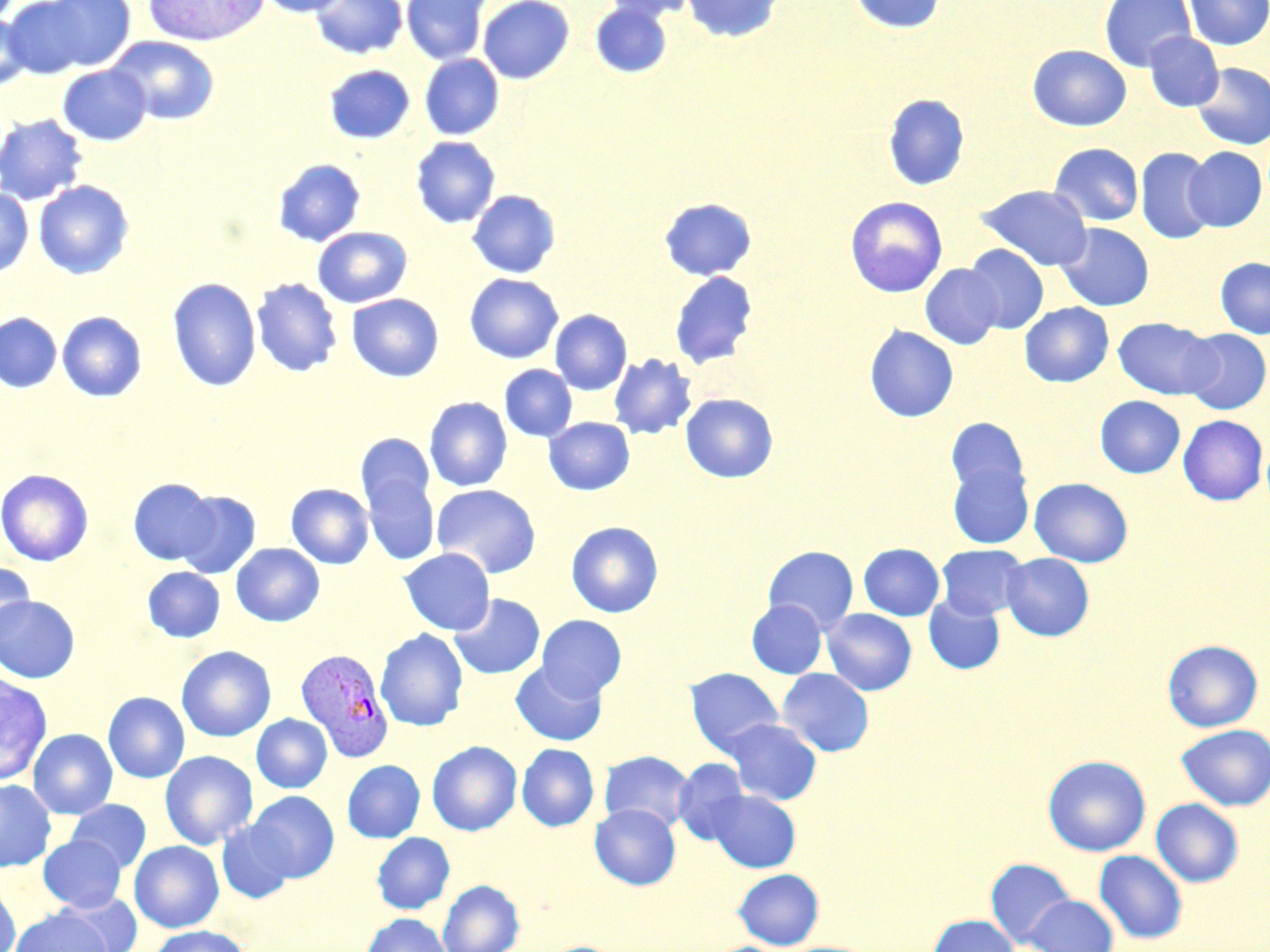

slide-level diagnosis = Plasmodium vivax
uninfected red blood cell locations = approximate bounding boxes as named x1/y1/x2/y2 corners in pixels: (x1=10, y1=0, x2=137, y2=75), (x1=143, y1=0, x2=268, y2=47), (x1=257, y1=0, x2=351, y2=17), (x1=310, y1=0, x2=407, y2=59), (x1=402, y1=0, x2=490, y2=65), (x1=478, y1=0, x2=574, y2=84), (x1=601, y1=0, x2=699, y2=22), (x1=681, y1=0, x2=785, y2=43), (x1=847, y1=0, x2=947, y2=35), (x1=1099, y1=0, x2=1195, y2=71), (x1=1183, y1=0, x2=1269, y2=51), (x1=589, y1=3, x2=672, y2=79), (x1=0, y1=12, x2=33, y2=89), (x1=1145, y1=32, x2=1224, y2=112), (x1=107, y1=36, x2=220, y2=125), (x1=1027, y1=44, x2=1131, y2=131), (x1=420, y1=54, x2=504, y2=140), (x1=1192, y1=62, x2=1270, y2=150), (x1=324, y1=64, x2=415, y2=144), (x1=58, y1=65, x2=152, y2=145), (x1=882, y1=93, x2=970, y2=191), (x1=0, y1=113, x2=89, y2=206), (x1=410, y1=136, x2=500, y2=228), (x1=1049, y1=143, x2=1144, y2=226), (x1=1183, y1=146, x2=1267, y2=231), (x1=1135, y1=147, x2=1217, y2=244), (x1=272, y1=158, x2=366, y2=247), (x1=33, y1=180, x2=135, y2=280), (x1=976, y1=184, x2=1092, y2=271), (x1=0, y1=188, x2=33, y2=277), (x1=467, y1=190, x2=560, y2=279), (x1=844, y1=196, x2=948, y2=297), (x1=659, y1=198, x2=757, y2=281), (x1=1056, y1=222, x2=1154, y2=311), (x1=312, y1=227, x2=412, y2=308), (x1=962, y1=245, x2=1049, y2=334), (x1=1215, y1=257, x2=1270, y2=338), (x1=920, y1=264, x2=1004, y2=349), (x1=669, y1=271, x2=758, y2=369), (x1=464, y1=273, x2=563, y2=363), (x1=167, y1=277, x2=261, y2=391), (x1=251, y1=278, x2=342, y2=377), (x1=346, y1=293, x2=444, y2=382), (x1=1019, y1=302, x2=1114, y2=387), (x1=550, y1=309, x2=632, y2=395), (x1=57, y1=311, x2=147, y2=402), (x1=0, y1=313, x2=61, y2=392), (x1=1113, y1=317, x2=1219, y2=400), (x1=864, y1=326, x2=958, y2=422), (x1=1181, y1=328, x2=1269, y2=414), (x1=608, y1=354, x2=697, y2=439), (x1=499, y1=364, x2=577, y2=442), (x1=680, y1=393, x2=778, y2=483), (x1=1095, y1=395, x2=1185, y2=478), (x1=424, y1=397, x2=512, y2=491), (x1=1178, y1=414, x2=1268, y2=505), (x1=544, y1=417, x2=634, y2=495), (x1=945, y1=417, x2=1031, y2=504), (x1=356, y1=433, x2=434, y2=518), (x1=947, y1=459, x2=1034, y2=549), (x1=0, y1=469, x2=93, y2=566), (x1=362, y1=470, x2=440, y2=565), (x1=1029, y1=477, x2=1133, y2=566), (x1=128, y1=478, x2=218, y2=565), (x1=286, y1=483, x2=374, y2=569), (x1=431, y1=484, x2=541, y2=578), (x1=173, y1=490, x2=261, y2=578), (x1=565, y1=521, x2=664, y2=617), (x1=231, y1=543, x2=325, y2=627), (x1=858, y1=543, x2=944, y2=620), (x1=937, y1=544, x2=1029, y2=619), (x1=762, y1=545, x2=859, y2=634), (x1=399, y1=548, x2=495, y2=635), (x1=1001, y1=553, x2=1094, y2=641), (x1=0, y1=562, x2=36, y2=646), (x1=142, y1=566, x2=225, y2=643), (x1=450, y1=594, x2=545, y2=679), (x1=923, y1=594, x2=1005, y2=674), (x1=0, y1=595, x2=80, y2=683), (x1=747, y1=599, x2=827, y2=678), (x1=822, y1=608, x2=917, y2=695), (x1=536, y1=615, x2=627, y2=698), (x1=375, y1=628, x2=468, y2=731), (x1=1162, y1=639, x2=1263, y2=732), (x1=176, y1=645, x2=276, y2=742), (x1=511, y1=660, x2=607, y2=746), (x1=685, y1=667, x2=784, y2=756), (x1=777, y1=668, x2=874, y2=757), (x1=0, y1=674, x2=53, y2=784), (x1=103, y1=692, x2=190, y2=783), (x1=252, y1=714, x2=332, y2=793), (x1=723, y1=718, x2=822, y2=805), (x1=1176, y1=724, x2=1270, y2=810), (x1=28, y1=729, x2=117, y2=819), (x1=427, y1=741, x2=522, y2=836), (x1=516, y1=743, x2=599, y2=832), (x1=160, y1=750, x2=258, y2=850), (x1=599, y1=750, x2=694, y2=832), (x1=1043, y1=755, x2=1151, y2=856), (x1=673, y1=758, x2=750, y2=845), (x1=342, y1=760, x2=425, y2=842), (x1=0, y1=779, x2=56, y2=872), (x1=709, y1=790, x2=800, y2=872), (x1=247, y1=791, x2=339, y2=882), (x1=1151, y1=798, x2=1243, y2=887), (x1=67, y1=799, x2=151, y2=874), (x1=590, y1=804, x2=681, y2=889), (x1=217, y1=819, x2=296, y2=903), (x1=372, y1=832, x2=455, y2=914), (x1=38, y1=836, x2=126, y2=913), (x1=129, y1=840, x2=224, y2=932), (x1=1094, y1=850, x2=1188, y2=944), (x1=985, y1=858, x2=1076, y2=947), (x1=732, y1=868, x2=823, y2=949), (x1=438, y1=879, x2=524, y2=952), (x1=0, y1=882, x2=21, y2=952), (x1=56, y1=891, x2=143, y2=952), (x1=1023, y1=894, x2=1118, y2=952), (x1=10, y1=906, x2=113, y2=952), (x1=362, y1=913, x2=452, y2=952), (x1=928, y1=914, x2=1018, y2=952), (x1=147, y1=925, x2=251, y2=952)
preparation = thin blood smear
field of view = single
stain = May-Grünwald-Giemsa
magnification = 1000x
image size = 1270×952 pixels
modality = optical microscopy
Plasmodium vivax-infected red blood cell locations = approximate bounding boxes as named x1/y1/x2/y2 corners in pixels: (x1=295, y1=648, x2=394, y2=762)